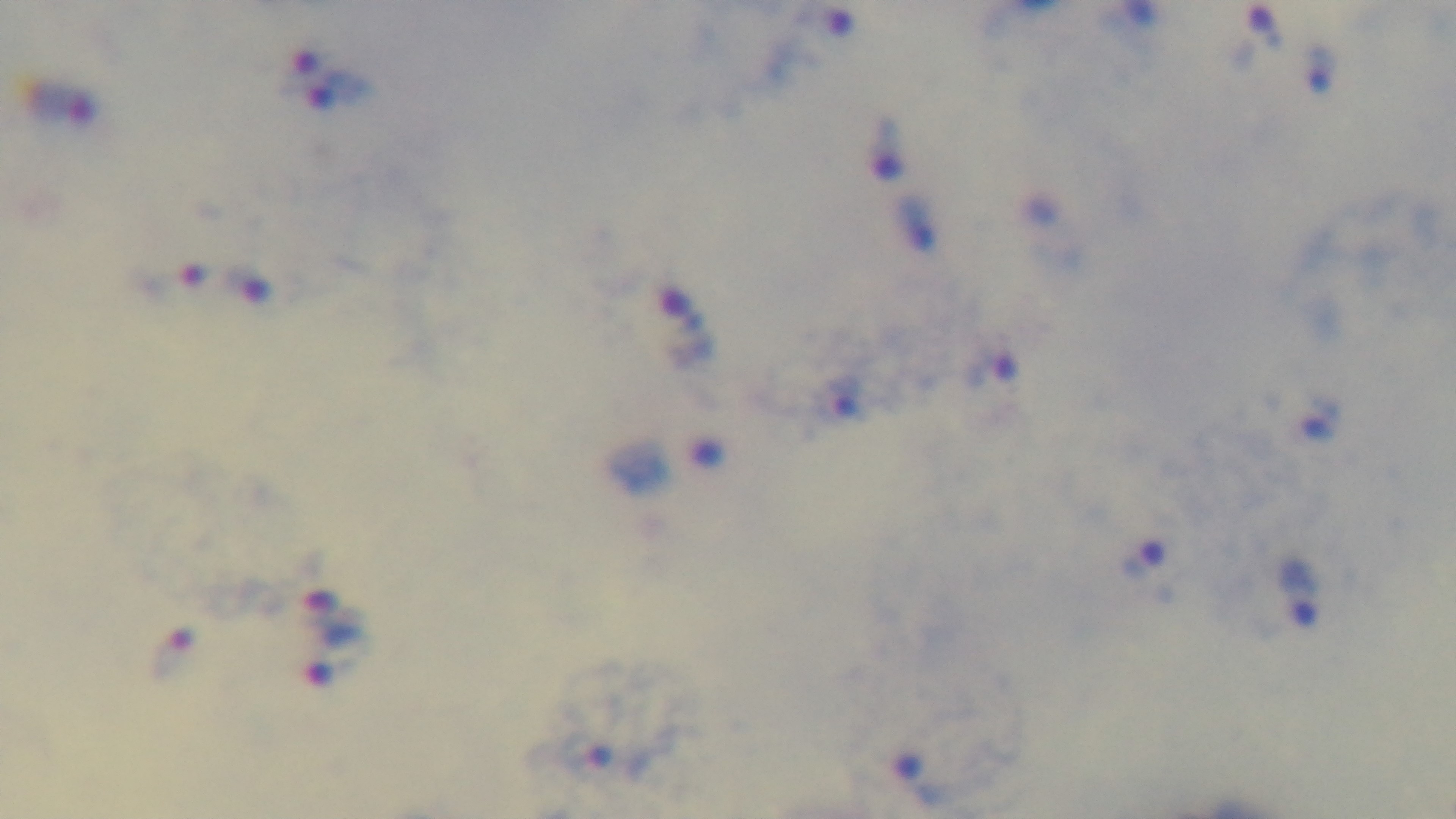
Preparation: thick smear. 100x oil-immersion objective. Photomicrograph. Giemsa-stained. One field from the slide. Malaria status: positive. Mounted 4K digital camera.